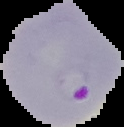
malaria_status: parasitized
image_type: cell region segmented out of the field of view; surrounding area masked to black
image_size: 124×127 pixels
preparation: thin blood smear